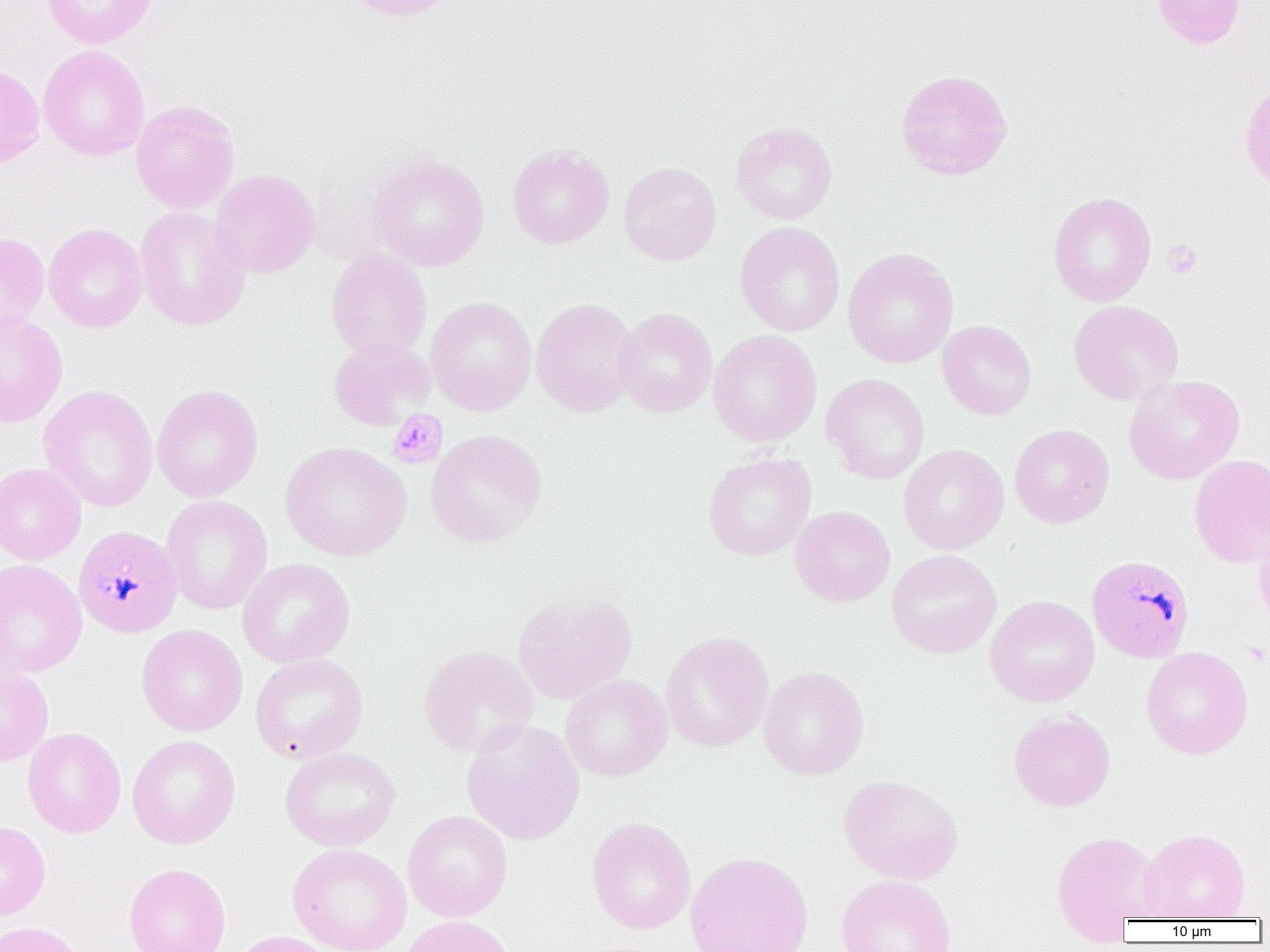
Approximate bounding boxes as (x1,y1)-(x2,y2) corner pairs in pixels. Platelet locations: (1163,239)-(1202,279), (387,409)-(448,469), (1245,642)-(1269,667). Uninfected red blood cell locations: (41,0)-(157,49), (339,0)-(458,22), (1151,0)-(1246,48), (38,44)-(151,161), (0,63)-(45,170), (894,68)-(1014,181), (1239,79)-(1270,196), (131,99)-(240,214), (731,121)-(837,224), (508,144)-(614,249), (369,154)-(490,271), (618,161)-(722,265), (209,169)-(321,279), (1048,191)-(1157,306), (134,205)-(251,331), (734,221)-(845,337), (44,223)-(147,333), (0,231)-(50,335), (843,248)-(959,368), (326,249)-(432,360), (426,296)-(537,416), (532,298)-(641,416), (1069,300)-(1184,404), (614,308)-(717,417), (0,311)-(67,428), (937,320)-(1036,420), (708,329)-(822,447), (330,338)-(435,429), (820,373)-(930,484), (1124,375)-(1245,485), (37,384)-(158,511), (151,384)-(264,503), (1010,424)-(1115,528), (426,429)-(548,548), (280,441)-(411,561), (898,444)-(1009,554), (703,451)-(817,560), (1189,454)-(1270,568), (0,463)-(86,565), (161,495)-(272,615), (790,506)-(895,606), (1253,519)-(1270,629), (886,549)-(1002,659), (0,558)-(87,678), (236,558)-(356,668), (512,591)-(637,704), (985,595)-(1100,707), (136,624)-(248,737), (661,632)-(773,753), (419,646)-(538,758), (1141,646)-(1253,759), (249,654)-(368,764), (0,666)-(54,766), (758,666)-(869,780), (560,674)-(672,781), (1009,710)-(1115,811), (462,719)-(585,845), (22,727)-(126,838), (127,734)-(240,849), (279,747)-(400,851), (838,774)-(964,885), (402,810)-(513,922), (586,817)-(696,935), (0,821)-(50,920), (1137,828)-(1251,921), (1051,830)-(1162,938), (287,843)-(412,952), (684,851)-(813,952), (123,862)-(231,952), (835,874)-(957,952), (399,915)-(516,952), (0,921)-(88,952), (230,930)-(337,952). Plasmodium malariae-infected red blood cell locations: (73,525)-(183,637), (1087,554)-(1194,663). Slide-level diagnosis: Plasmodium malariae. One field of a larger specimen. Thin blood film. Light microscopy. Image is 1270×952 pixels. 1000x magnification.